Assess this cell for malaria.
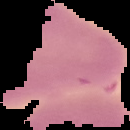

It is uninfected.

image_size: 130×130 pixels
image_type: segmented cell region with the area outside set to black
preparation: thin blood smear